Assess this cell for malaria.
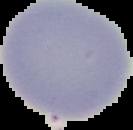

Uninfected.

Image is 133×130 pixels. The area outside the segmented cell region is set to black. From a thin blood film.